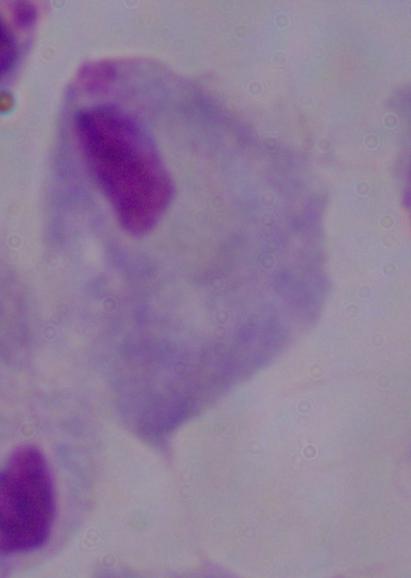
Summary:
  - Magnification: 1000x
  - Identification: trichomonad
  - Modality: photomicrograph